State which parasite is depicted.
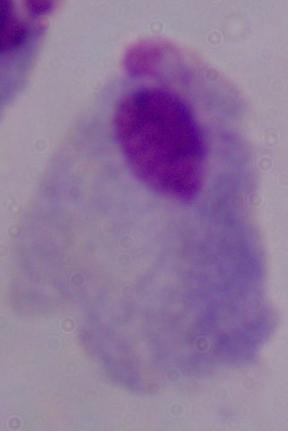

This is a trichomonad.

magnification = 1000x
modality = micrograph